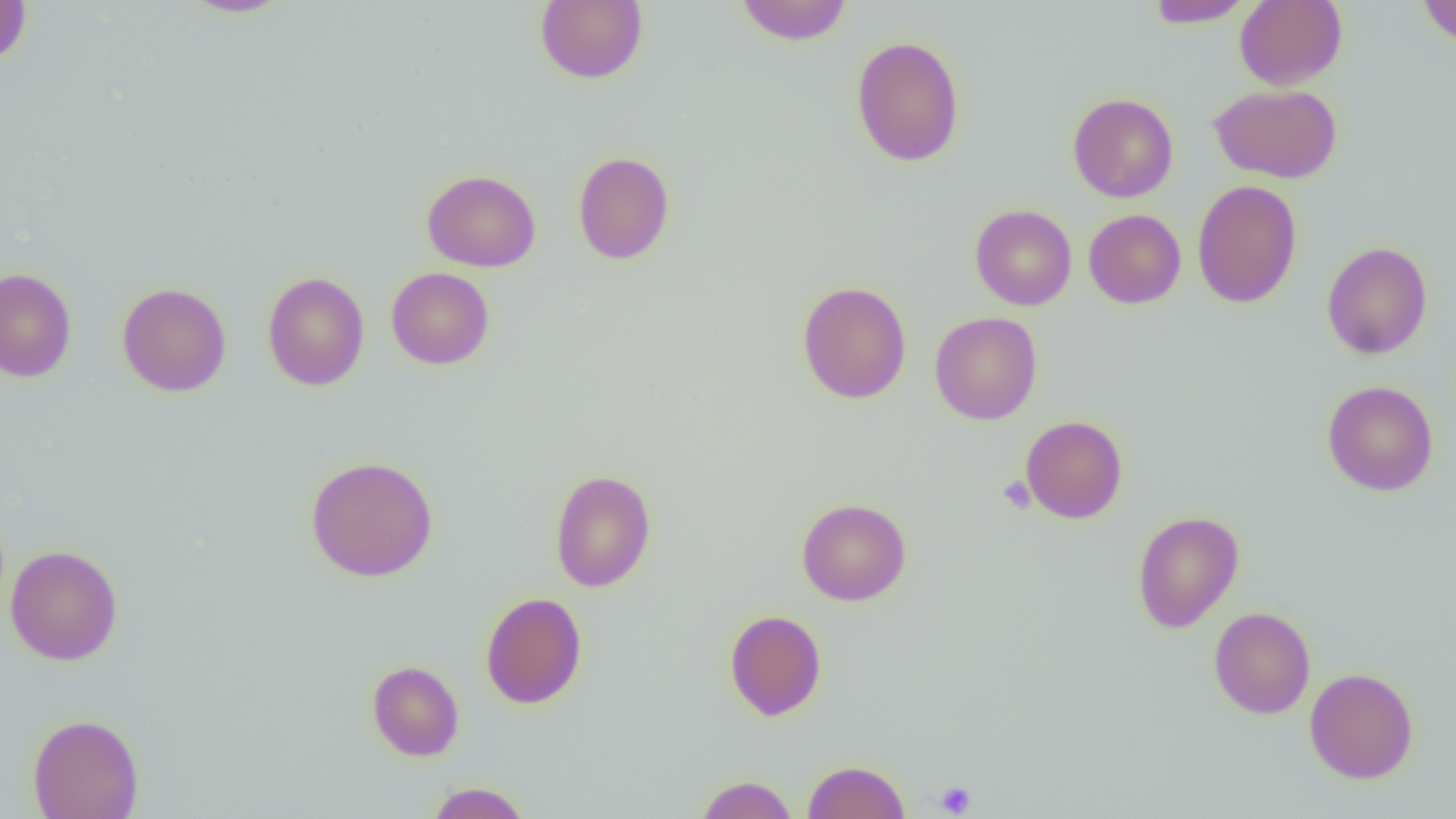
{
  "slide_level_diagnosis": "no evidence of blood parasites",
  "platelet_locations": "approximate bounding boxes as named x1/y1/x2/y2 corners in pixels: (x1=998, y1=476, x2=1035, y2=514), (x1=934, y1=780, x2=977, y2=817)",
  "modality": "light microscopy",
  "uninfected_red_blood_cell_locations": "approximate bounding boxes as named x1/y1/x2/y2 corners in pixels: (x1=180, y1=0, x2=292, y2=18), (x1=535, y1=0, x2=648, y2=84), (x1=735, y1=0, x2=852, y2=45), (x1=1145, y1=0, x2=1252, y2=27), (x1=1235, y1=0, x2=1347, y2=90), (x1=1417, y1=0, x2=1456, y2=46), (x1=0, y1=1, x2=32, y2=66), (x1=851, y1=35, x2=965, y2=167), (x1=1209, y1=83, x2=1342, y2=183), (x1=1068, y1=93, x2=1178, y2=202), (x1=573, y1=151, x2=675, y2=265), (x1=422, y1=169, x2=541, y2=272), (x1=1192, y1=179, x2=1302, y2=309), (x1=970, y1=204, x2=1077, y2=310), (x1=1083, y1=209, x2=1186, y2=309), (x1=1321, y1=241, x2=1432, y2=359), (x1=386, y1=267, x2=494, y2=370), (x1=0, y1=268, x2=76, y2=382), (x1=263, y1=271, x2=369, y2=391), (x1=796, y1=280, x2=911, y2=404), (x1=117, y1=282, x2=232, y2=396), (x1=930, y1=312, x2=1042, y2=425), (x1=1322, y1=380, x2=1438, y2=496), (x1=1020, y1=415, x2=1128, y2=524), (x1=305, y1=455, x2=438, y2=582), (x1=549, y1=469, x2=656, y2=592), (x1=796, y1=498, x2=911, y2=606), (x1=1132, y1=511, x2=1243, y2=633), (x1=5, y1=544, x2=122, y2=665), (x1=480, y1=592, x2=587, y2=708), (x1=1209, y1=606, x2=1315, y2=719), (x1=724, y1=610, x2=827, y2=721), (x1=367, y1=660, x2=464, y2=761), (x1=1304, y1=667, x2=1418, y2=784), (x1=28, y1=713, x2=144, y2=819), (x1=802, y1=759, x2=910, y2=819), (x1=696, y1=775, x2=797, y2=818), (x1=426, y1=781, x2=532, y2=818)",
  "field_of_view": "one of a larger specimen",
  "image_size": "1456×819 pixels",
  "magnification": "1000x",
  "preparation": "thin blood film"
}